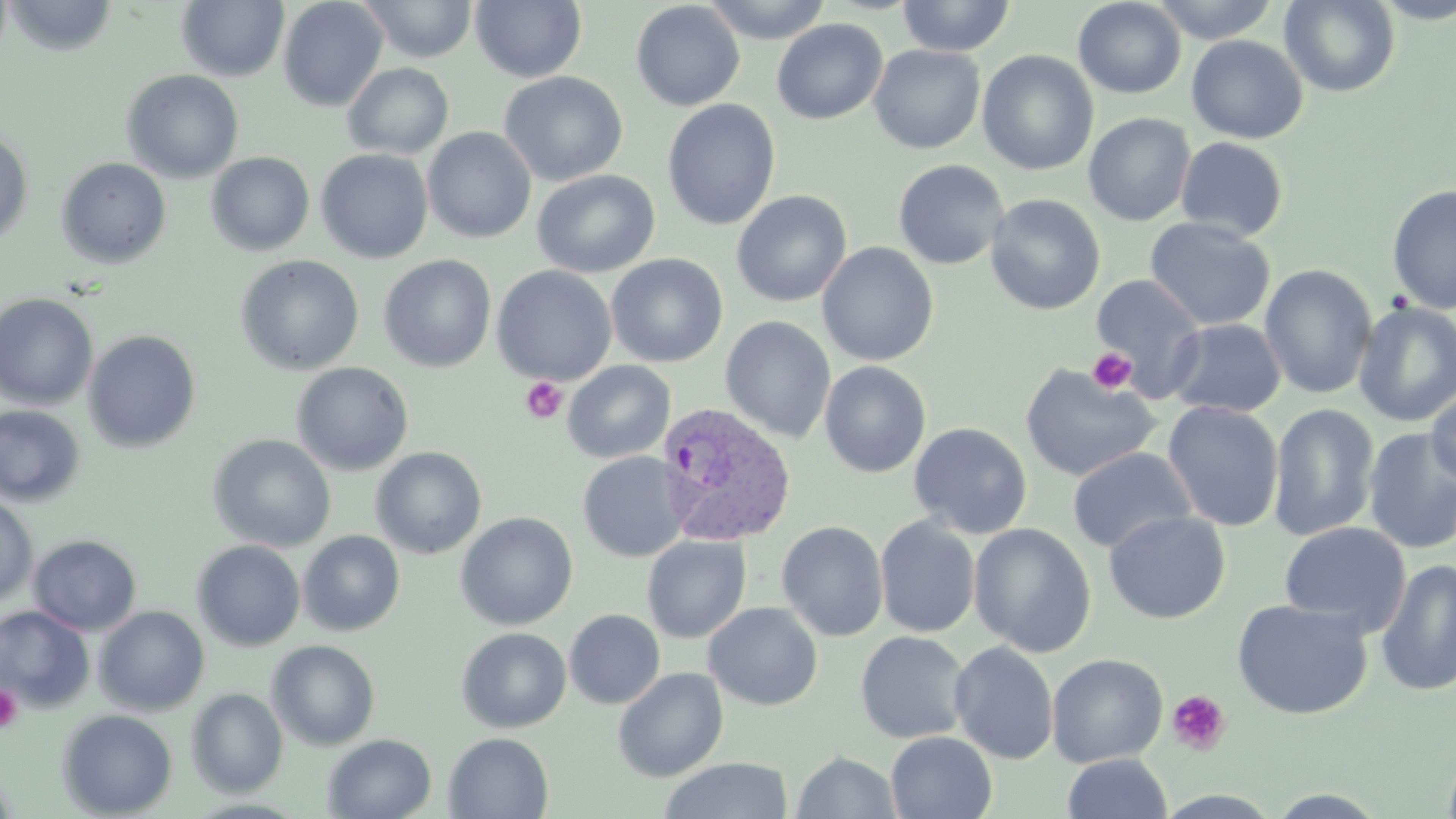

Summary:
  - Coordinate format: approximate bounding boxes as (x1,y1)-(x2,y2) corner pairs in pixels
  - Platelet locations: (1087,346)-(1137,394), (520,377)-(568,424), (0,684)-(23,732), (1166,690)-(1231,755)
  - Uninfected red blood cell locations: (5,0)-(117,56), (176,0)-(290,82), (277,0)-(388,111), (358,0)-(478,62), (471,0)-(586,83), (700,0)-(833,43), (896,0)-(1016,56), (1073,0)-(1186,98), (1149,0)-(1281,43), (1372,0)-(1456,24), (631,1)-(745,111), (1280,1)-(1399,96), (772,19)-(887,124), (1186,35)-(1308,144), (868,44)-(985,154), (976,50)-(1099,175), (343,63)-(454,159), (121,69)-(244,183), (499,71)-(627,187), (662,99)-(780,230), (1083,113)-(1196,226), (423,127)-(537,243), (0,131)-(33,246), (1175,136)-(1289,241), (316,149)-(433,263), (206,152)-(314,256), (56,158)-(171,269), (893,159)-(1009,269), (532,169)-(660,278), (1386,183)-(1456,314), (732,190)-(851,307), (985,194)-(1105,315), (1144,217)-(1276,331), (817,242)-(938,366), (236,254)-(364,375), (378,254)-(497,373), (606,254)-(728,367), (1260,263)-(1378,399), (492,265)-(616,385), (1090,274)-(1206,396), (0,293)-(98,410), (1353,301)-(1456,427), (720,316)-(836,443), (1165,318)-(1286,417), (83,330)-(201,452), (820,360)-(931,478), (562,361)-(675,463), (292,362)-(413,476), (1019,362)-(1161,482), (1425,384)-(1456,488), (1162,401)-(1284,532), (1267,403)-(1380,543), (0,405)-(85,508), (909,422)-(1032,539), (1362,427)-(1456,554), (209,434)-(336,553), (371,447)-(487,559), (1067,447)-(1197,554), (578,452)-(688,562), (0,493)-(38,607), (1103,510)-(1230,624), (455,512)-(578,630), (875,516)-(980,637), (776,520)-(889,641), (1278,521)-(1412,636), (969,523)-(1096,657), (299,530)-(405,636), (28,534)-(141,635), (642,535)-(751,643), (192,540)-(305,651), (1376,559)-(1456,696), (1232,598)-(1373,720), (703,602)-(822,710), (0,606)-(95,712), (94,606)-(209,715), (564,609)-(665,709), (457,627)-(571,733), (855,630)-(972,744), (267,640)-(380,750), (949,641)-(1059,764), (1047,653)-(1168,767), (613,667)-(728,781), (186,688)-(288,798), (57,709)-(177,817), (885,732)-(997,818), (444,733)-(553,818), (323,734)-(437,818), (1443,742)-(1456,819), (791,751)-(902,818), (1062,753)-(1173,818), (657,758)-(794,819), (1262,789)-(1392,818)
  - Plasmodium vivax-infected red blood cell locations: (657,404)-(797,547)
  - Slide-level diagnosis: Plasmodium vivax
  - Magnification: 1000x
  - Stain: May-Grünwald-Giemsa
  - Field of view: one of a larger specimen
  - Preparation: thin blood smear
  - Modality: optical microscopy
  - Image size: 1456×819 pixels